Assess this cell for malaria.
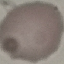

Uninfected.

Summary:
  - Image type: automatically extracted cell patch, resized to 64 × 64 pixels
  - Capture: smartphone camera at the microscope eyepiece
  - Preparation: thin blood film
  - Stain: Giemsa